Point out every malaria parasite.
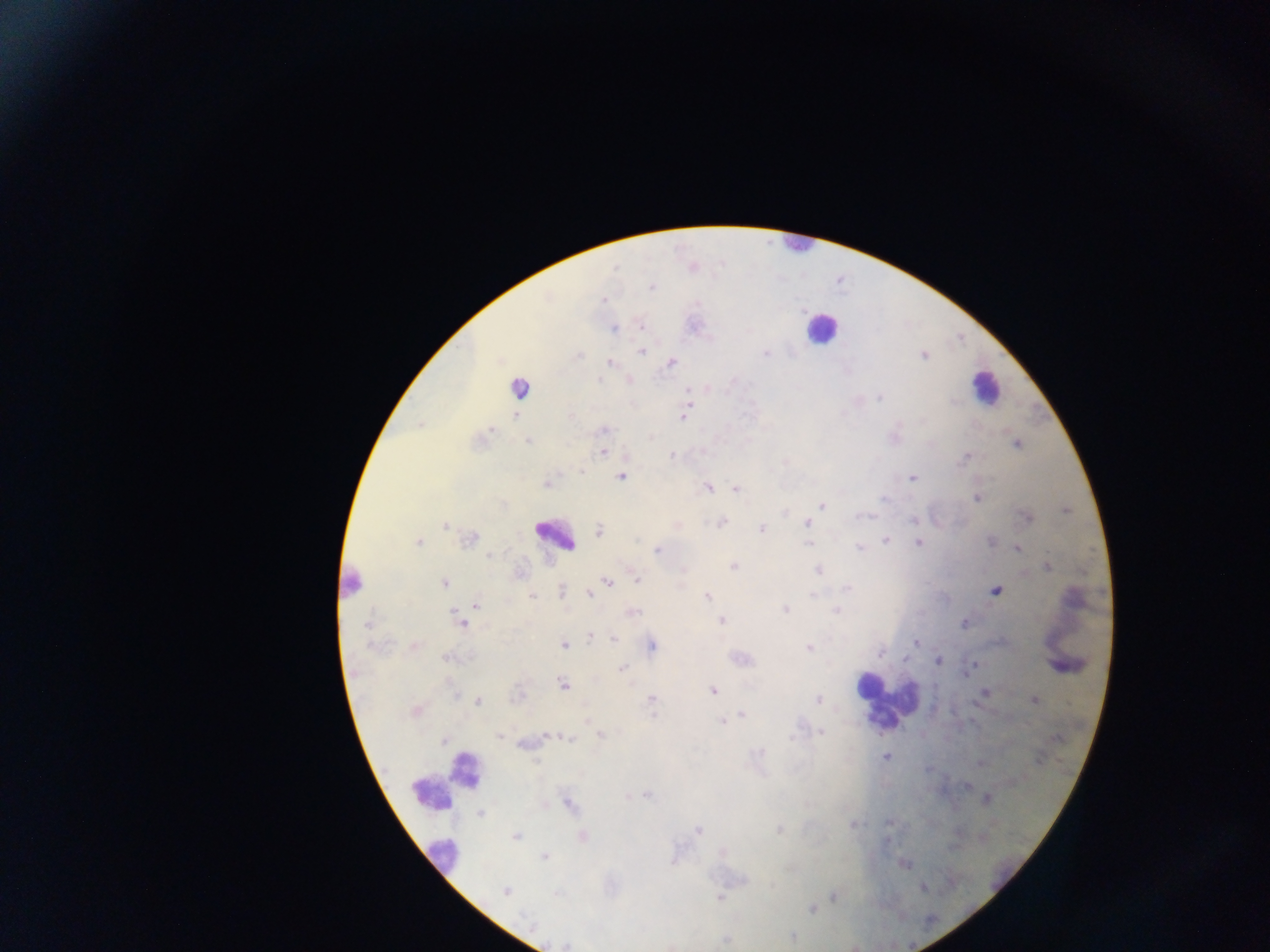

Approximate centers as x y in pixels.
Malaria parasites: 615 269; 652 287; 603 299; 641 327; 614 329; 641 352; 765 354; 579 355; 924 356; 671 362; 610 363; 598 380; 687 389; 880 397; 515 415; 571 416; 683 418; 491 430; 603 430; 527 442; 1016 445; 603 452; 671 456; 966 456; 582 471; 621 477; 912 478; 546 484; 708 488; 736 489; 977 498; 884 499; 822 506; 1067 510; 863 515; 1026 517; 913 520; 721 523; 807 523; 446 526; 762 528; 599 530; 470 539; 886 540; 991 541; 418 542; 918 542; 809 543; 859 548; 1017 548; 658 550; 488 555; 733 567; 1047 567; 817 570; 636 578; 351 580; 607 580; 444 583; 847 588; 561 591; 996 591; 589 593; 814 595; 532 596; 707 596; 476 604; 784 609; 634 611; 836 611; 456 615; 721 621; 461 623; 965 623; 366 626; 590 636; 615 639; 915 643; 564 645; 414 646; 653 646; 808 649; 880 653; 446 658; 937 660; 972 666; 623 668; 562 685; 713 691; 985 692; 455 694; 651 700; 818 700; 1034 700; 478 701; 416 711; 653 714; 742 714; 587 720; 722 721; 821 732; 601 735; 499 736; 570 739; 759 753; 886 757; 536 761; 980 763; 966 785; 647 795; 569 804; 481 814; 853 824; 780 830; 698 831; 516 836; 583 836; 544 856; 923 887; 505 891; 556 894; 834 897; 719 898; 812 909; 792 938.

preparation = thick blood film
capture = mobile-phone photograph through a microscope
field of view = single
image size = 1270×952 pixels
country = Ghana
leukocyte locations = approximate centers as x y in pixels: 796 246; 821 329; 517 387; 985 387; 558 537; 866 684; 887 702; 445 782; 444 856